Name the parasite shown.
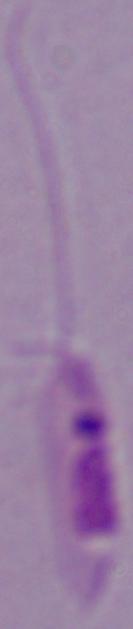

This is Leishmania.

modality = photomicrograph
magnification = 1000x